Classify this cell by malaria status.
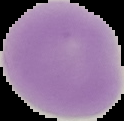

Uninfected.

Image is 124×121 pixels. From a thin blood film. Cell region segmented out of the field of view; the surrounding area is masked to black.